Classify this cell by malaria status.
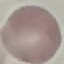
Uninfected.

{
  "capture": "smartphone through the microscope eyepiece",
  "stain": "Giemsa",
  "image_type": "cell patch, automatically extracted from a larger field of view and resized to 64 × 64 pixels",
  "preparation": "thin blood film"
}